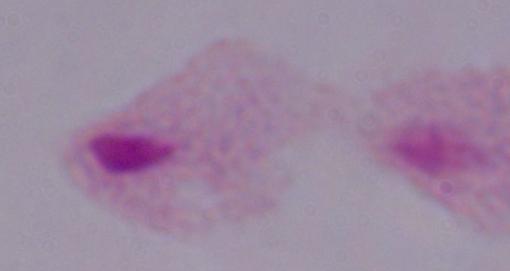

magnification: 1000x
modality: photomicrograph
identification: trichomonad